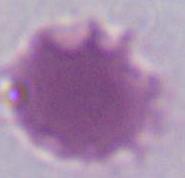

Summary:
  - Modality: photomicrograph
  - Magnification: 1000x
  - Identification: erythrocyte